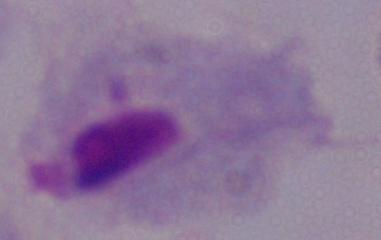
identification = trichomonad
magnification = 1000x
modality = photomicrograph